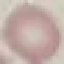

{
  "result": "no malaria parasites seen",
  "preparation": "thin blood film",
  "stain": "Giemsa",
  "image_type": "cell patch, automatically extracted from a larger field of view and resized to 64 × 64 pixels",
  "capture": "smartphone camera at the microscope eyepiece"
}